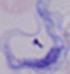
magnification = 1000x
identification = trypanosome
modality = micrograph